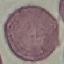

Result: no malaria parasites detected. Giemsa-stained preparation. Photographed with a smartphone camera at the microscope eyepiece. Cell patch, automatically extracted from a larger field of view and resized to 64 × 64 pixels. Thin blood smear.